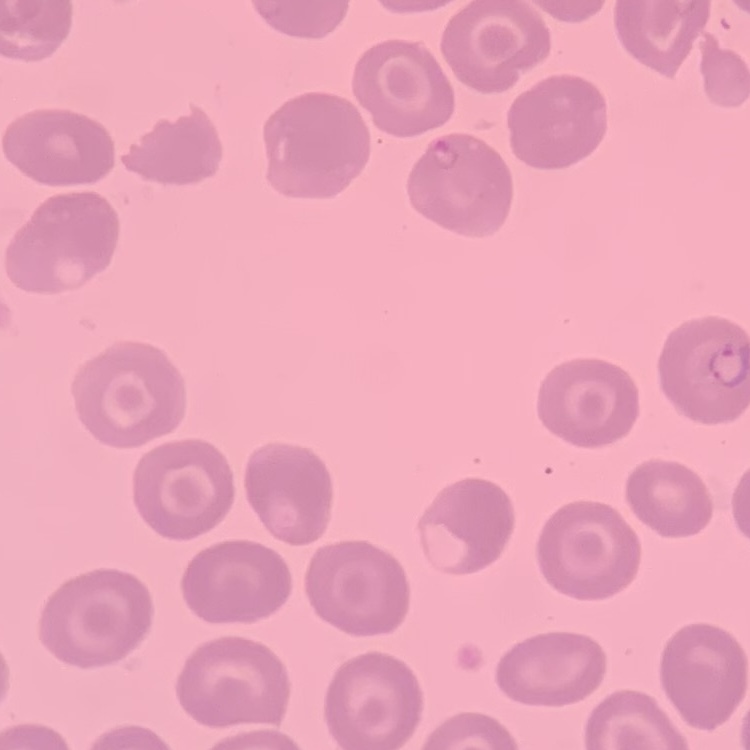

Summary:
  - Erythrocyte morphology: no rouleaux formation
  - Stain: Field's or Giemsa
  - Image type: one tile cut from a larger photomicrograph
  - Preparation: thin blood film